Give the extent of all Plasmodium vivax-infected red blood cells.
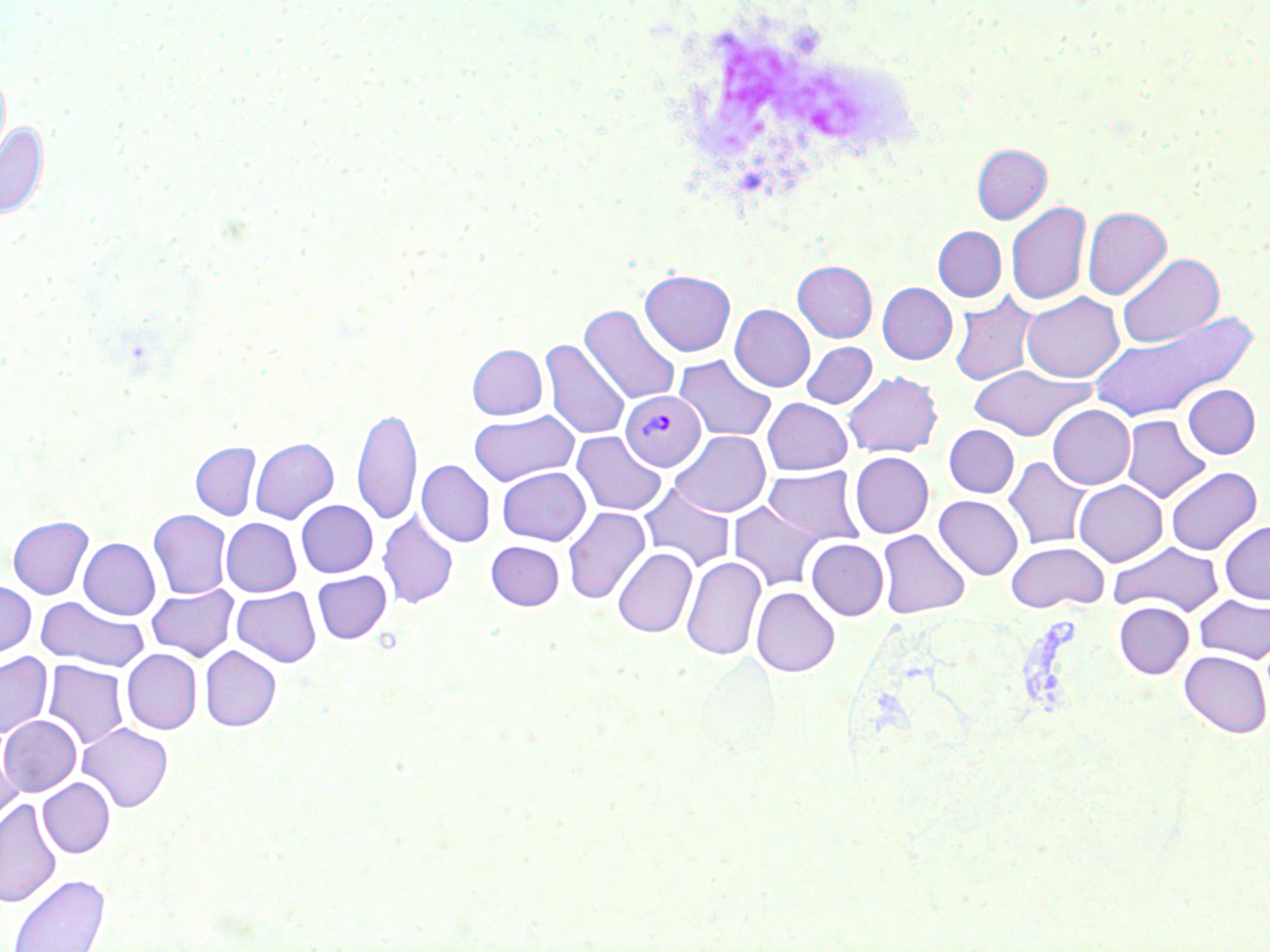
Approximate bounding boxes as named x1/y1/x2/y2 corners in pixels.
Plasmodium vivax-infected red blood cells: (x1=621, y1=391, x2=705, y2=471).

{
  "slide_level_diagnosis": "Plasmodium vivax",
  "image_size": "1270×952 pixels",
  "field_of_view": "one of a larger specimen",
  "white_blood_cell_locations": "approximate bounding boxes as named x1/y1/x2/y2 corners in pixels: (x1=683, y1=20, x2=941, y2=187)",
  "uninfected_red_blood_cell_locations": "approximate bounding boxes as named x1/y1/x2/y2 corners in pixels: (x1=0, y1=65, x2=11, y2=166), (x1=0, y1=122, x2=49, y2=220), (x1=972, y1=144, x2=1051, y2=224), (x1=1006, y1=201, x2=1090, y2=306), (x1=1082, y1=207, x2=1171, y2=300), (x1=933, y1=226, x2=1006, y2=302), (x1=1116, y1=252, x2=1224, y2=349), (x1=793, y1=260, x2=877, y2=342), (x1=640, y1=269, x2=736, y2=356), (x1=877, y1=283, x2=957, y2=364), (x1=949, y1=291, x2=1041, y2=387), (x1=1022, y1=292, x2=1124, y2=382), (x1=580, y1=303, x2=681, y2=405), (x1=730, y1=304, x2=815, y2=392), (x1=1087, y1=313, x2=1257, y2=421), (x1=541, y1=338, x2=630, y2=440), (x1=802, y1=341, x2=877, y2=408), (x1=468, y1=344, x2=546, y2=419), (x1=673, y1=354, x2=777, y2=442), (x1=967, y1=365, x2=1094, y2=440), (x1=843, y1=370, x2=943, y2=457), (x1=1183, y1=384, x2=1260, y2=459), (x1=762, y1=398, x2=852, y2=475), (x1=1047, y1=405, x2=1135, y2=489), (x1=353, y1=406, x2=421, y2=525), (x1=470, y1=410, x2=578, y2=486), (x1=1121, y1=415, x2=1211, y2=503), (x1=944, y1=425, x2=1019, y2=498), (x1=671, y1=430, x2=771, y2=517), (x1=572, y1=431, x2=666, y2=516), (x1=250, y1=438, x2=338, y2=523), (x1=191, y1=442, x2=260, y2=520), (x1=849, y1=452, x2=933, y2=538), (x1=1004, y1=456, x2=1092, y2=550), (x1=417, y1=460, x2=495, y2=547), (x1=497, y1=466, x2=590, y2=545), (x1=762, y1=466, x2=865, y2=545), (x1=1165, y1=466, x2=1262, y2=555), (x1=1074, y1=480, x2=1168, y2=566), (x1=639, y1=481, x2=736, y2=571), (x1=933, y1=495, x2=1023, y2=580), (x1=296, y1=500, x2=377, y2=577), (x1=728, y1=500, x2=825, y2=591), (x1=562, y1=506, x2=650, y2=605), (x1=148, y1=510, x2=231, y2=599), (x1=378, y1=510, x2=458, y2=608), (x1=8, y1=516, x2=93, y2=599), (x1=222, y1=518, x2=301, y2=596), (x1=1219, y1=520, x2=1270, y2=604), (x1=877, y1=529, x2=969, y2=618), (x1=79, y1=538, x2=160, y2=619), (x1=806, y1=538, x2=889, y2=620), (x1=486, y1=541, x2=564, y2=610), (x1=1005, y1=541, x2=1109, y2=612), (x1=1108, y1=541, x2=1225, y2=617), (x1=613, y1=547, x2=697, y2=637), (x1=681, y1=556, x2=765, y2=661), (x1=312, y1=571, x2=391, y2=644), (x1=0, y1=580, x2=35, y2=659), (x1=146, y1=584, x2=239, y2=661), (x1=232, y1=587, x2=320, y2=667), (x1=751, y1=587, x2=840, y2=677), (x1=1194, y1=594, x2=1270, y2=664), (x1=35, y1=596, x2=149, y2=672), (x1=1113, y1=602, x2=1194, y2=678), (x1=200, y1=645, x2=281, y2=731), (x1=122, y1=649, x2=202, y2=734), (x1=1179, y1=650, x2=1270, y2=738), (x1=0, y1=652, x2=52, y2=738), (x1=42, y1=660, x2=129, y2=750), (x1=0, y1=715, x2=81, y2=796), (x1=77, y1=723, x2=173, y2=812), (x1=0, y1=738, x2=22, y2=829), (x1=38, y1=778, x2=114, y2=857), (x1=0, y1=798, x2=62, y2=908), (x1=7, y1=873, x2=111, y2=952)",
  "modality": "optical microscopy",
  "preparation": "thin blood film",
  "magnification": "1000x",
  "stain": "May-Grünwald-Giemsa"
}